Locate every blood parasite and identify its species.
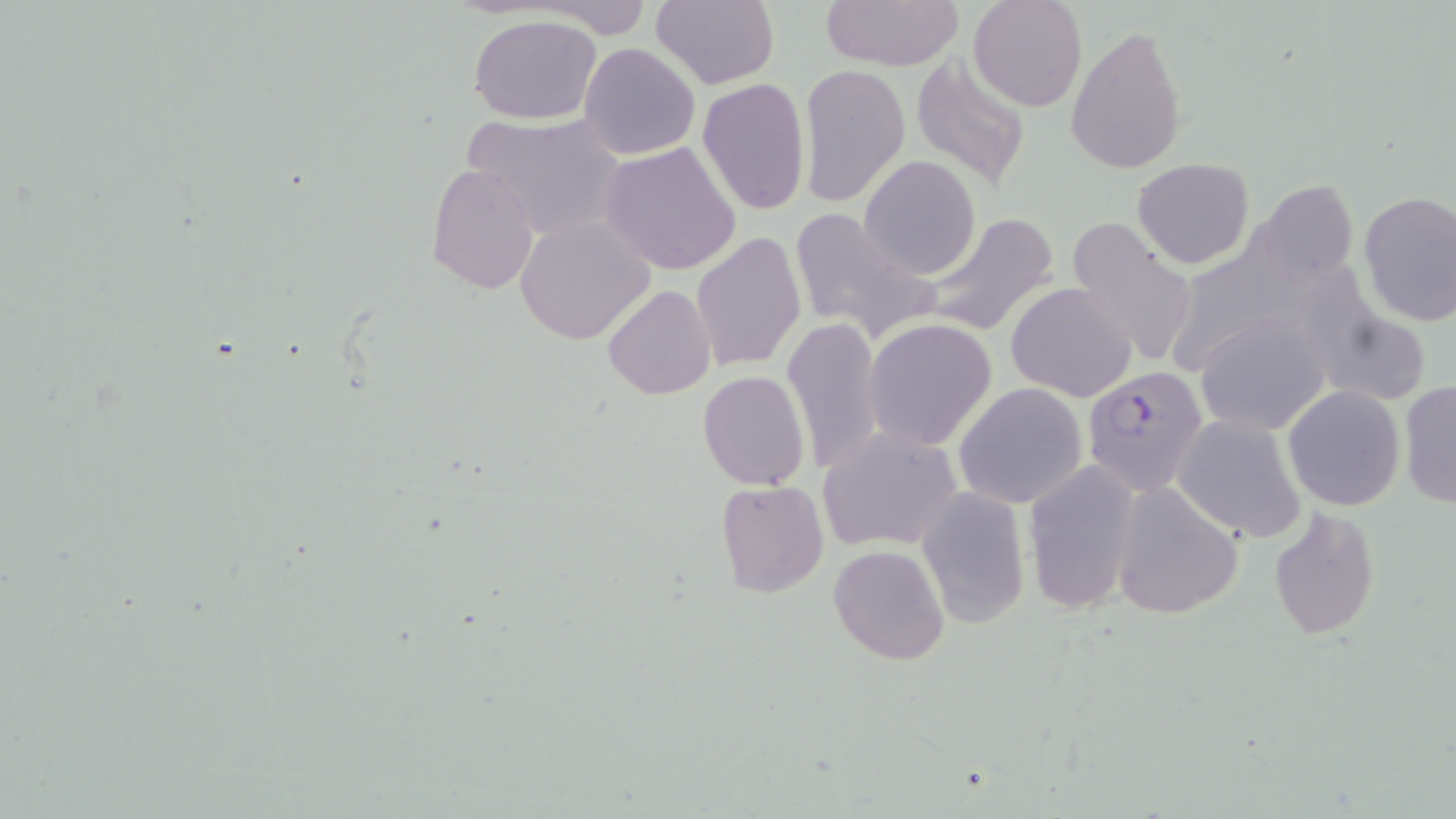
Approximate bounding boxes as named x1/y1/x2/y2 corners in pixels.
Plasmodium falciparum-infected red blood cells: (x1=1080, y1=367, x2=1208, y2=497).
No Plasmodium ovale, Plasmodium malariae, Plasmodium vivax, Babesia divergens, or Trypanosoma brucei observed.

{
  "slide_level_diagnosis": "Plasmodium falciparum",
  "uninfected_red_blood_cell_locations": "approximate bounding boxes as named x1/y1/x2/y2 corners in pixels: (x1=651, y1=0, x2=780, y2=89), (x1=817, y1=0, x2=964, y2=70), (x1=967, y1=0, x2=1086, y2=112), (x1=529, y1=2, x2=661, y2=37), (x1=465, y1=14, x2=605, y2=124), (x1=1065, y1=23, x2=1188, y2=175), (x1=578, y1=41, x2=700, y2=161), (x1=910, y1=54, x2=1032, y2=189), (x1=797, y1=63, x2=911, y2=208), (x1=697, y1=76, x2=812, y2=214), (x1=459, y1=111, x2=631, y2=242), (x1=598, y1=141, x2=742, y2=275), (x1=860, y1=154, x2=982, y2=279), (x1=1134, y1=159, x2=1255, y2=268), (x1=427, y1=163, x2=541, y2=297), (x1=1356, y1=189, x2=1456, y2=327), (x1=788, y1=207, x2=934, y2=342), (x1=916, y1=211, x2=1061, y2=337), (x1=514, y1=215, x2=654, y2=344), (x1=1066, y1=220, x2=1201, y2=371), (x1=692, y1=231, x2=806, y2=372), (x1=1317, y1=277, x2=1432, y2=405), (x1=1007, y1=281, x2=1139, y2=402), (x1=603, y1=284, x2=715, y2=400), (x1=1195, y1=313, x2=1331, y2=436), (x1=780, y1=315, x2=889, y2=474), (x1=865, y1=317, x2=998, y2=451), (x1=697, y1=370, x2=811, y2=490), (x1=1398, y1=380, x2=1456, y2=511), (x1=955, y1=384, x2=1088, y2=508), (x1=1283, y1=385, x2=1405, y2=511), (x1=1173, y1=414, x2=1309, y2=544), (x1=815, y1=427, x2=964, y2=554), (x1=1021, y1=460, x2=1141, y2=614), (x1=715, y1=481, x2=829, y2=600), (x1=1108, y1=481, x2=1244, y2=620), (x1=916, y1=487, x2=1030, y2=628), (x1=1268, y1=507, x2=1380, y2=638), (x1=829, y1=544, x2=949, y2=665)",
  "modality": "optical microscopy",
  "preparation": "thin blood smear",
  "field_of_view": "one of a larger specimen",
  "magnification": "1000x",
  "image_size": "1456×819 pixels",
  "stain": "May-Grünwald-Giemsa"
}